Comment on the morphology of the erythrocytes.
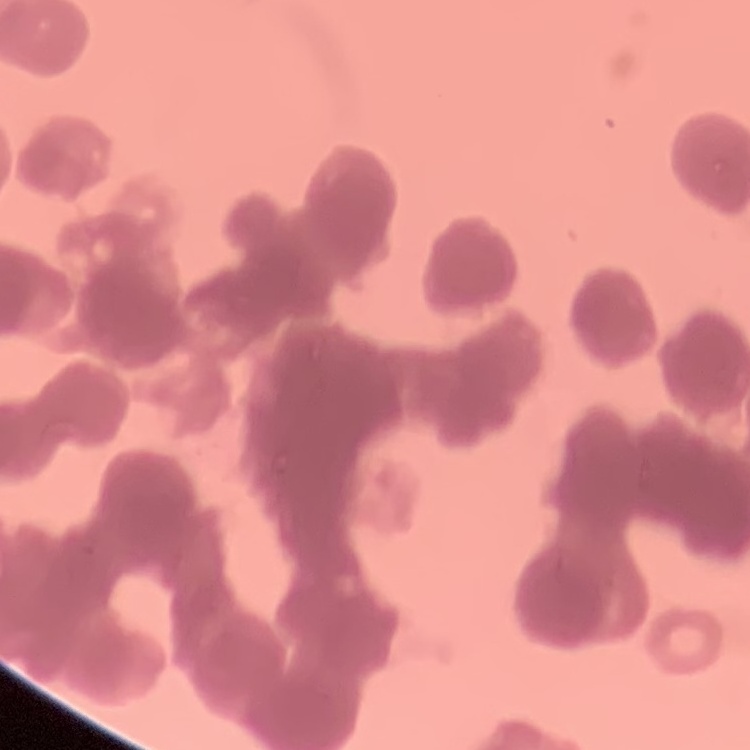

They show rouleaux formation.

Summary:
  - Stain: Field's or Giemsa
  - Preparation: thin blood film
  - Image type: one tile cut from a larger photomicrograph